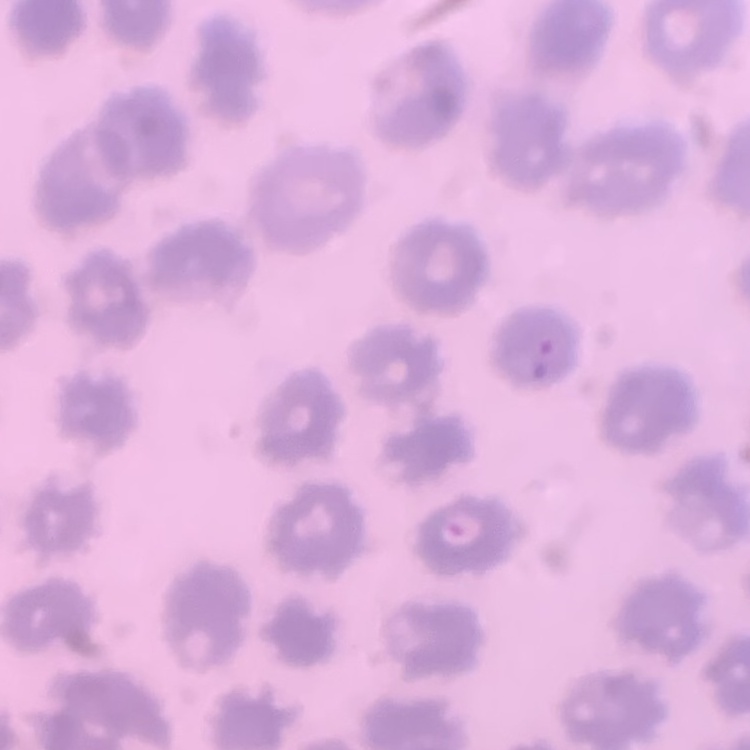
erythrocyte_morphology: no rouleaux formation
stain: Field's or Giemsa
image_type: square crop of a larger photomicrograph
preparation: thin blood film